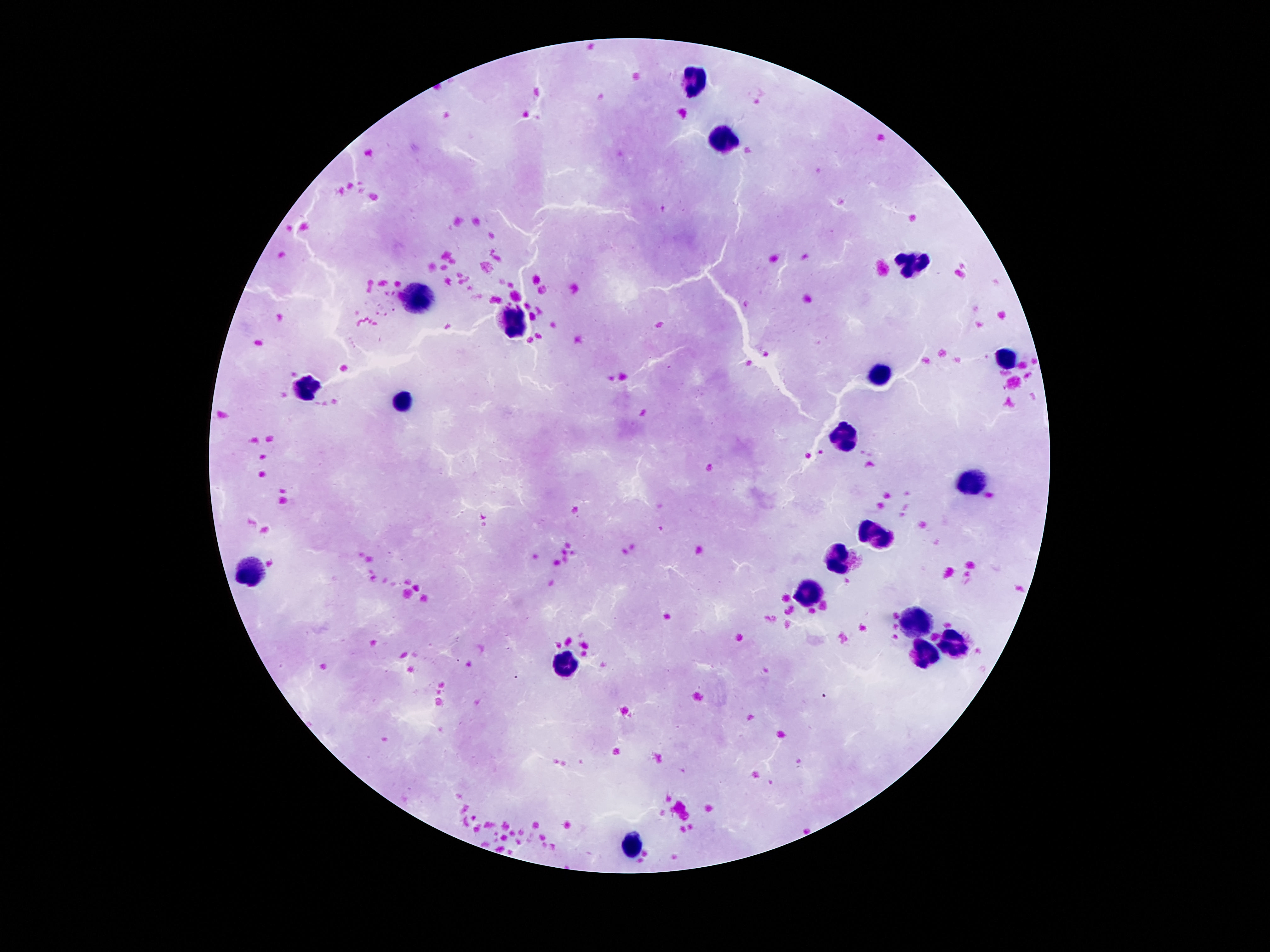
Approximate object centers, in pixels from the top-left corner. Leukocyte locations: (x=694, y=79), (x=726, y=134), (x=909, y=262), (x=411, y=298), (x=513, y=320), (x=1005, y=359), (x=878, y=375), (x=307, y=385), (x=405, y=402), (x=847, y=437), (x=972, y=484), (x=878, y=537), (x=839, y=559), (x=247, y=572), (x=808, y=591), (x=917, y=624), (x=956, y=644), (x=923, y=650), (x=563, y=663), (x=632, y=846). Photographed through the microscope eyepiece with a smartphone camera. Single field of view. Thick peripheral-blood smear. 100x magnification. Patient malaria status: negative. Image is 1270×952 pixels. Giemsa-stained preparation.